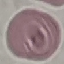
Summary:
  - Malaria status: uninfected
  - Stain: Giemsa
  - Preparation: thin blood film
  - Capture: smartphone through the microscope eyepiece
  - Image type: automatically extracted cell patch, resized to 64 × 64 pixels